Locate every Plasmodium parasite.
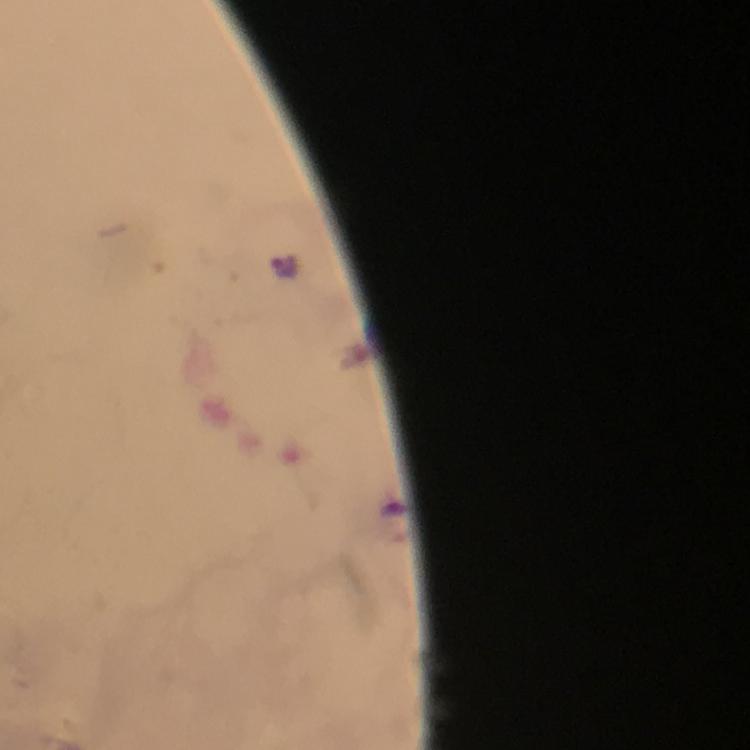

Approximate centers as [x, y] in pixels.
Plasmodium parasites: [285, 266].

Summary:
  - Immersion oil: applied
  - Preparation: thick smear
  - Capture: smartphone photograph through a microscope
  - Context: from a malaria diagnostic workup
  - Stain: Giemsa
  - Image size: 750×750 pixels
  - Cropped from: a single field of view
  - Magnification: 100x